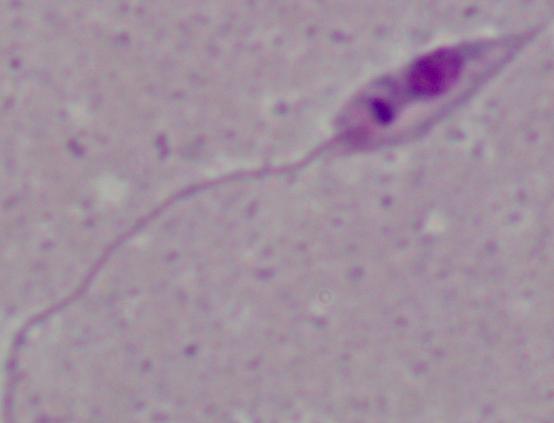 1000x magnification. A Leishmania parasite is seen. Photomicrograph.